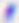
Summary:
  - Identification: Toxoplasma gondii
  - Modality: micrograph
  - Magnification: 400x